Locate every blood parasite and identify its species.
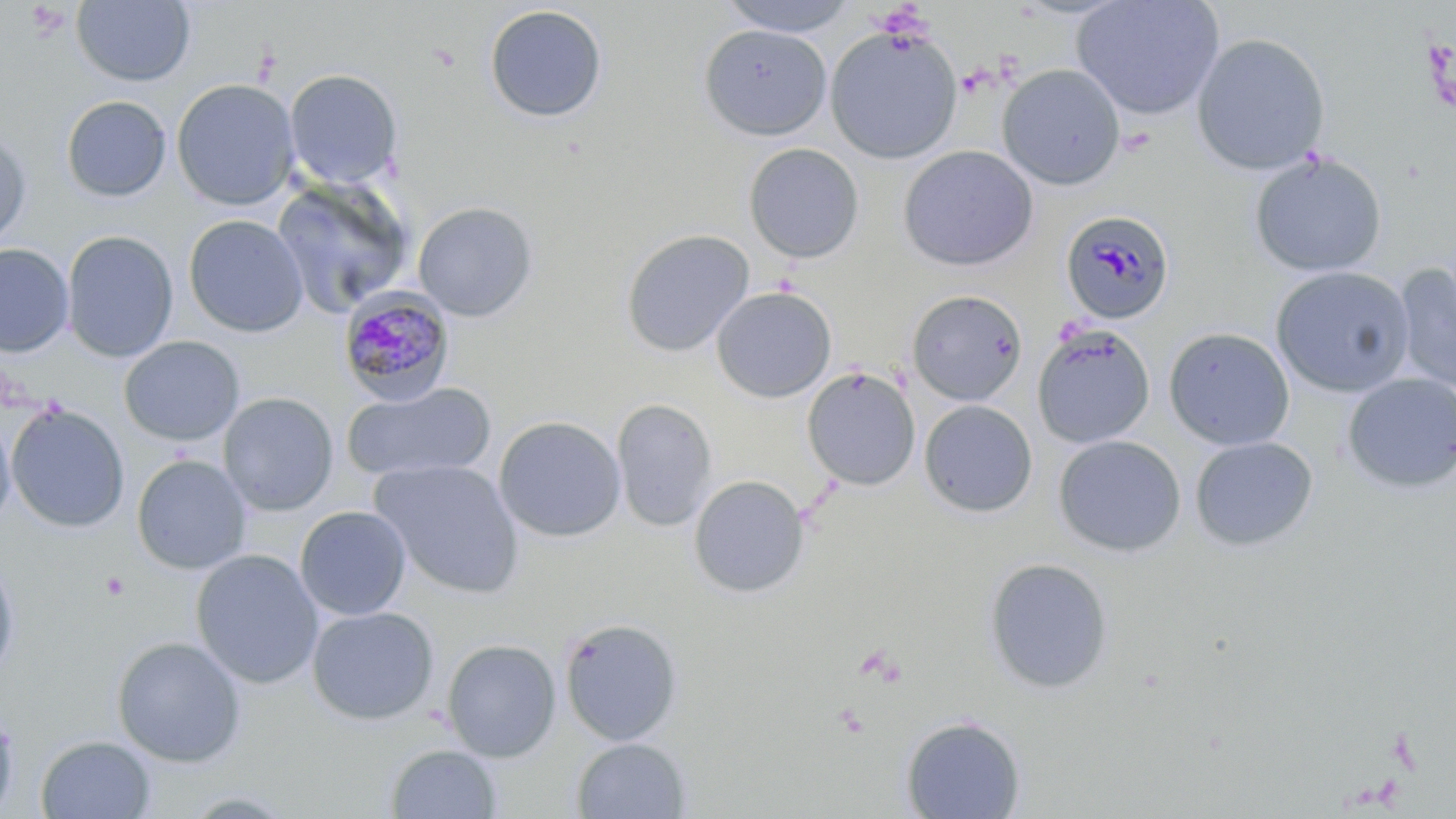

Approximate bounding boxes as [x1, y1, x2, y2] in pixels.
Plasmodium malariae-infected red blood cells: [1063, 214, 1172, 322], [337, 286, 456, 405].
No Plasmodium falciparum, Plasmodium ovale, Plasmodium vivax, Babesia divergens, or Trypanosoma brucei observed.

Platelet locations: [100, 572, 129, 601]. Uninfected red blood cell locations: [715, 0, 862, 37], [1070, 0, 1225, 120], [71, 1, 196, 87], [483, 4, 608, 123], [698, 23, 832, 141], [825, 26, 963, 164], [1191, 33, 1331, 176], [996, 64, 1127, 190], [284, 69, 403, 190], [171, 78, 300, 211], [61, 95, 172, 202], [0, 128, 32, 249], [743, 143, 865, 263], [897, 145, 1038, 272], [1249, 151, 1387, 278], [270, 178, 415, 320], [412, 201, 539, 322], [183, 214, 308, 337], [62, 227, 309, 352], [620, 228, 755, 358], [62, 230, 178, 362], [0, 242, 75, 358], [1393, 264, 1456, 395], [1270, 266, 1415, 397], [711, 286, 837, 403], [906, 289, 1029, 406], [1031, 324, 1155, 449], [1164, 327, 1295, 451], [119, 336, 245, 446], [801, 367, 921, 491], [1341, 373, 1456, 493], [342, 382, 497, 483], [218, 391, 338, 516], [611, 398, 718, 532], [918, 400, 1037, 518], [6, 404, 130, 533], [0, 412, 16, 531], [492, 415, 627, 542], [1053, 435, 1186, 558], [1190, 436, 1318, 552], [131, 454, 253, 576], [370, 459, 524, 598], [688, 474, 810, 599], [295, 506, 411, 621], [190, 548, 324, 689], [0, 556, 20, 684], [984, 558, 1114, 694], [306, 605, 439, 725], [559, 617, 684, 746], [111, 636, 248, 767], [441, 639, 561, 762], [0, 704, 19, 817], [900, 715, 1026, 819], [36, 734, 156, 819], [570, 737, 692, 818], [385, 743, 502, 818]. Slide-level diagnosis: Plasmodium malariae. Thin blood smear. Image is 1456×819 pixels. Optical microscopy. 1000x magnification. May-Grünwald-Giemsa stain. One field of a larger specimen.